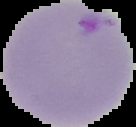 The area outside the segmented cell region is set to black. From a thin blood film. Image is 136×127 pixels. Malaria status: parasitized.